Identify the cell.
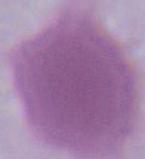
An erythrocyte.

Summary:
  - Magnification: 1000x
  - Modality: micrograph